Give the position of every malaria parasite.
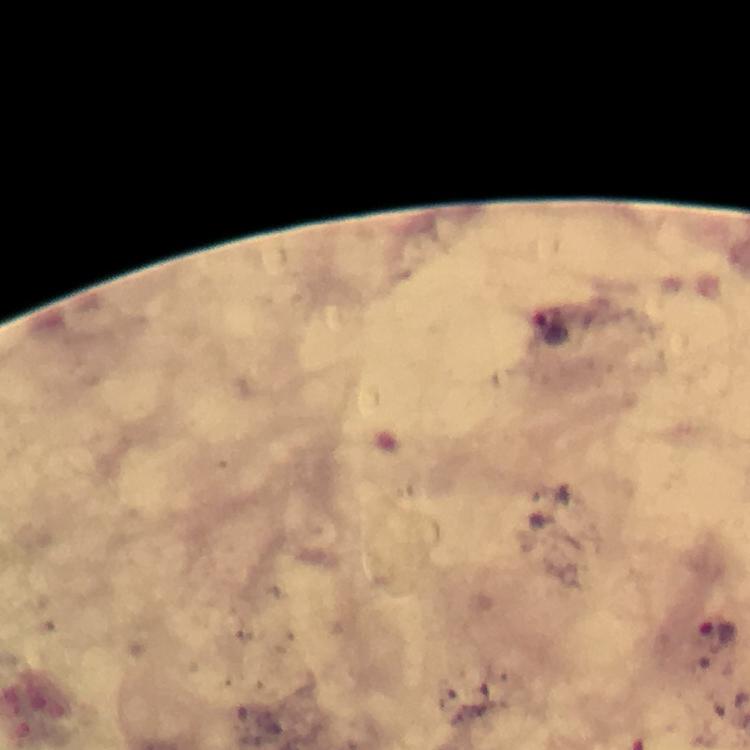

Approximate centers as [x, y] in pixels.
Malaria parasites: [552, 326], [721, 633].

Summary:
  - Context: from a malaria diagnostic workup
  - Preparation: thick blood smear
  - Immersion oil: applied
  - Stain: Giemsa
  - Cropped from: one field of view
  - Capture: smartphone camera through the microscope
  - Magnification: 100x
  - Image size: 750×750 pixels